Assess this cell for malaria.
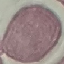
Uninfected.

preparation: thin blood film
capture: smartphone camera at the microscope eyepiece
image_type: automatically extracted cell patch, resized to 64 × 64 pixels
stain: Giemsa